Give the extent of all Plasmodium malariae-infected red blood cells.
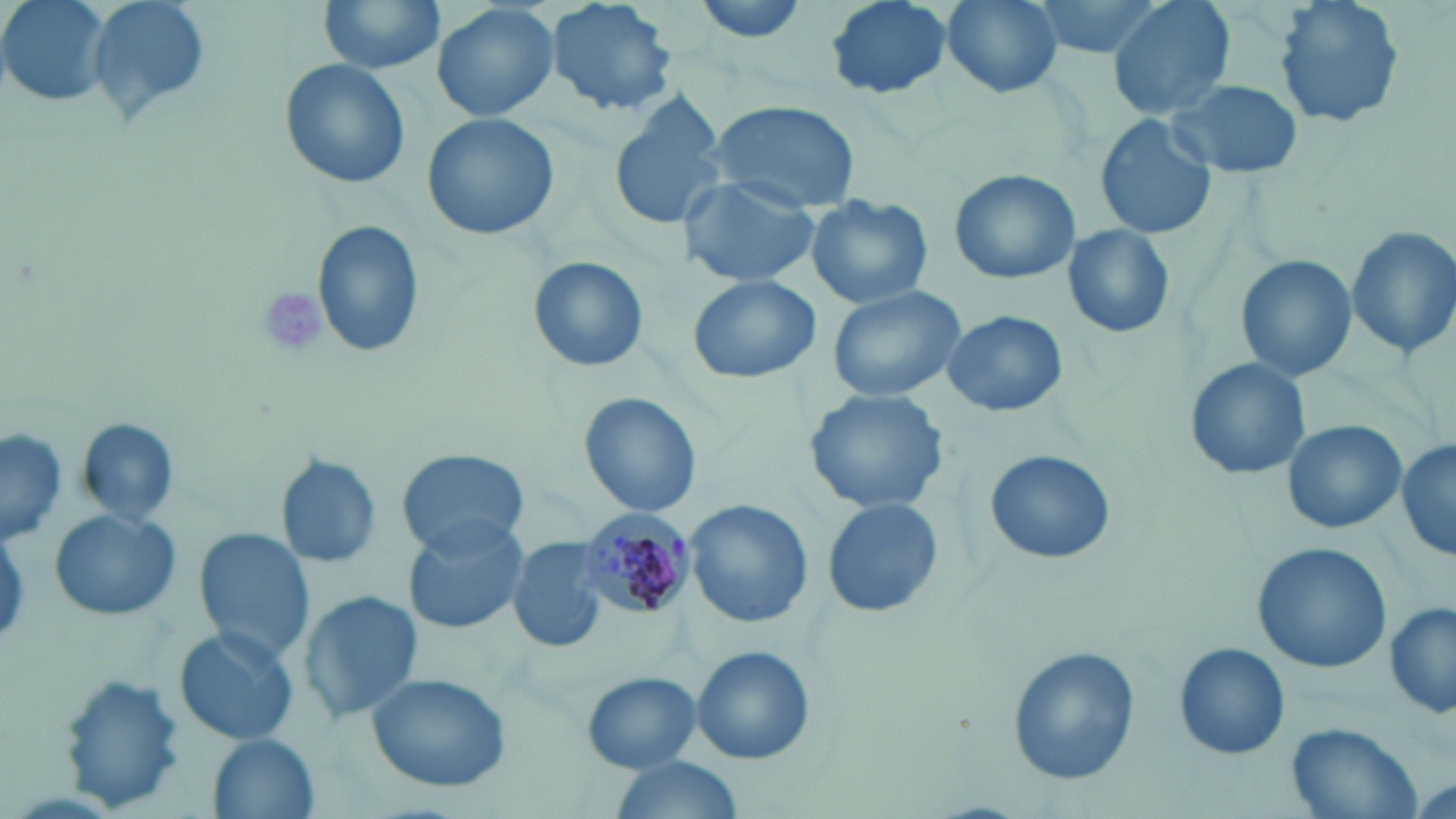
Approximate bounding boxes as named x1/y1/x2/y2 corners in pixels.
Plasmodium malariae-infected red blood cells: (x1=579, y1=509, x2=696, y2=621).

Summary:
  - Platelet locations: (x1=256, y1=288, x2=330, y2=360)
  - Uninfected red blood cell locations: (x1=1, y1=0, x2=111, y2=107), (x1=84, y1=0, x2=213, y2=132), (x1=317, y1=0, x2=446, y2=74), (x1=545, y1=0, x2=676, y2=117), (x1=690, y1=0, x2=812, y2=45), (x1=823, y1=0, x2=954, y2=101), (x1=936, y1=0, x2=1066, y2=98), (x1=1032, y1=0, x2=1171, y2=58), (x1=1105, y1=0, x2=1237, y2=120), (x1=1275, y1=0, x2=1404, y2=127), (x1=431, y1=1, x2=559, y2=123), (x1=281, y1=61, x2=408, y2=189), (x1=1168, y1=77, x2=1303, y2=179), (x1=608, y1=92, x2=728, y2=232), (x1=705, y1=100, x2=860, y2=211), (x1=422, y1=113, x2=560, y2=244), (x1=1095, y1=115, x2=1215, y2=240), (x1=949, y1=169, x2=1080, y2=286), (x1=679, y1=176, x2=819, y2=289), (x1=806, y1=194, x2=933, y2=309), (x1=314, y1=220, x2=426, y2=360), (x1=1061, y1=223, x2=1176, y2=339), (x1=1344, y1=225, x2=1456, y2=360), (x1=1235, y1=254, x2=1358, y2=383), (x1=530, y1=256, x2=648, y2=372), (x1=686, y1=273, x2=822, y2=385), (x1=827, y1=283, x2=972, y2=403), (x1=942, y1=309, x2=1068, y2=418), (x1=1185, y1=359, x2=1308, y2=479), (x1=805, y1=388, x2=951, y2=516), (x1=579, y1=394, x2=702, y2=519), (x1=77, y1=418, x2=181, y2=526), (x1=1280, y1=419, x2=1405, y2=535), (x1=1, y1=428, x2=65, y2=548), (x1=1395, y1=439, x2=1455, y2=562), (x1=398, y1=448, x2=528, y2=555), (x1=984, y1=448, x2=1116, y2=566), (x1=275, y1=453, x2=382, y2=570), (x1=821, y1=495, x2=945, y2=619), (x1=686, y1=501, x2=812, y2=628), (x1=48, y1=508, x2=181, y2=623), (x1=401, y1=515, x2=529, y2=634), (x1=191, y1=526, x2=317, y2=666), (x1=509, y1=537, x2=613, y2=654), (x1=1251, y1=541, x2=1391, y2=675), (x1=296, y1=590, x2=424, y2=726), (x1=1385, y1=602, x2=1455, y2=720), (x1=173, y1=626, x2=300, y2=748), (x1=1173, y1=643, x2=1289, y2=760), (x1=691, y1=645, x2=816, y2=765), (x1=1006, y1=645, x2=1139, y2=785), (x1=364, y1=670, x2=512, y2=793), (x1=581, y1=672, x2=701, y2=772), (x1=58, y1=674, x2=185, y2=813), (x1=1284, y1=723, x2=1421, y2=819), (x1=204, y1=733, x2=320, y2=819), (x1=607, y1=756, x2=746, y2=819)
  - Slide-level diagnosis: Plasmodium malariae
  - Image size: 1456×819 pixels
  - Stain: May-Grünwald-Giemsa
  - Field of view: one of a larger specimen
  - Magnification: 1000x
  - Preparation: thin blood film
  - Modality: light microscopy